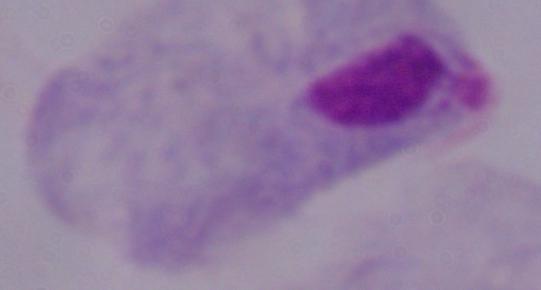 Photomicrograph. 1000x magnification. A trichomonad is seen.